Give the position of every leukocyte visible.
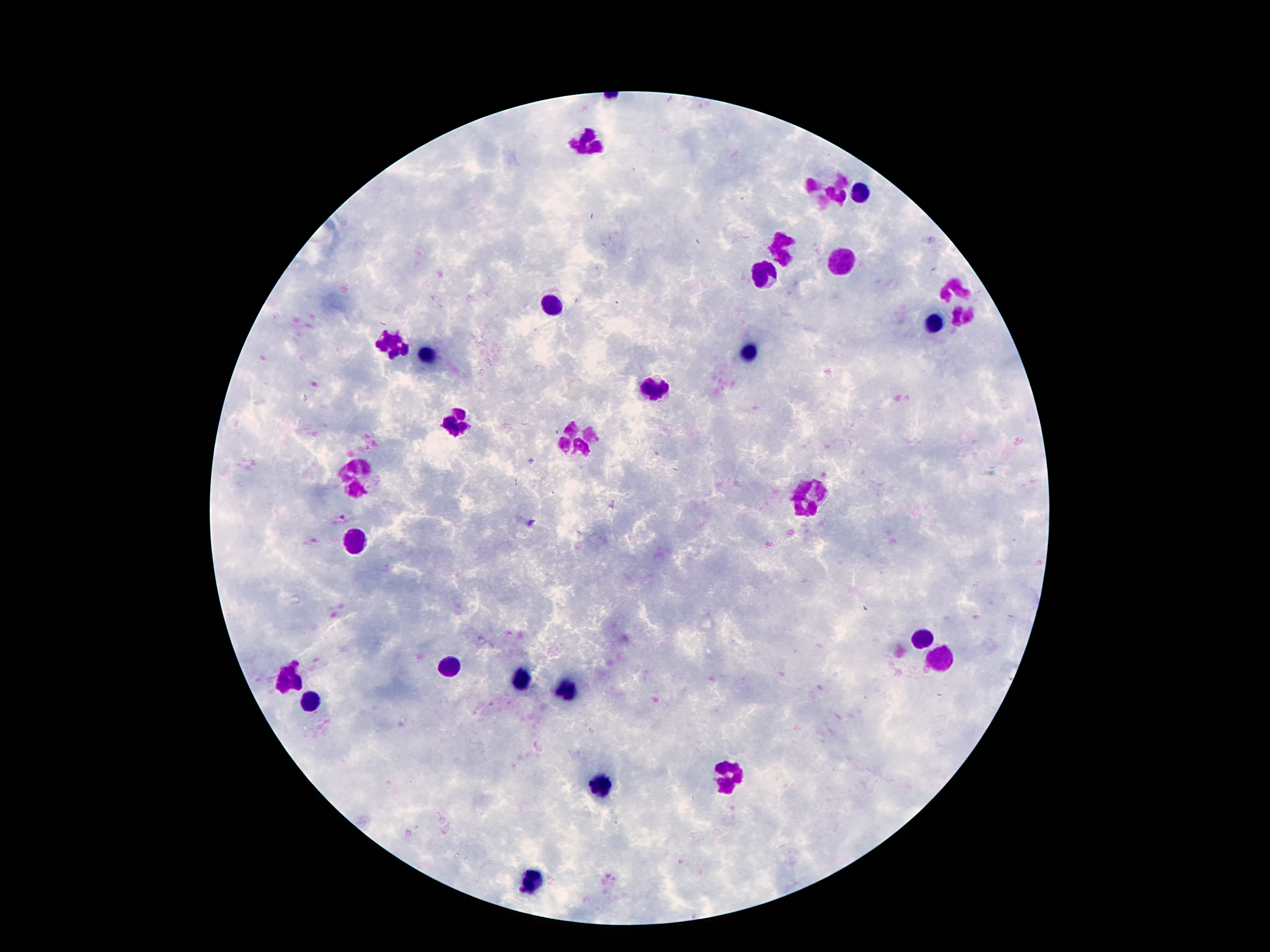
Approximate object centers, in pixels from the top-left corner.
Leukocytes: (x=587, y=141), (x=858, y=194), (x=832, y=195), (x=781, y=244), (x=842, y=262), (x=765, y=272), (x=954, y=289), (x=552, y=303), (x=963, y=319), (x=940, y=323), (x=396, y=340), (x=427, y=352), (x=753, y=353), (x=657, y=387), (x=457, y=424), (x=578, y=440), (x=355, y=475), (x=807, y=495), (x=357, y=540), (x=924, y=638), (x=940, y=660), (x=446, y=667), (x=287, y=679), (x=522, y=680), (x=567, y=692), (x=312, y=698), (x=730, y=774), (x=602, y=786), (x=531, y=879).

Summary:
  - Magnification: 100x
  - Preparation: thick peripheral-blood smear
  - Capture: smartphone camera through the microscope eyepiece
  - Patient malaria status: negative
  - Stain: Giemsa
  - Field of view: one from this slide
  - Image size: 1270×952 pixels